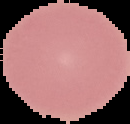
Summary:
  - Preparation: thin blood smear
  - Malaria status: uninfected
  - Image size: 130×124 pixels
  - Image type: segmented cell region on a black background